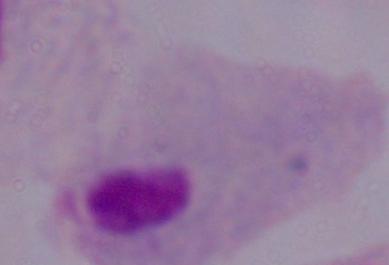
A trichomonad is seen. Micrograph. Captured at 1000x magnification.